Classify this cell by malaria status.
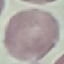
It is uninfected.

stain = Giemsa
image type = automatically extracted cell patch, resized to 64 × 64 pixels
capture = smartphone camera at the microscope eyepiece
preparation = thin blood smear